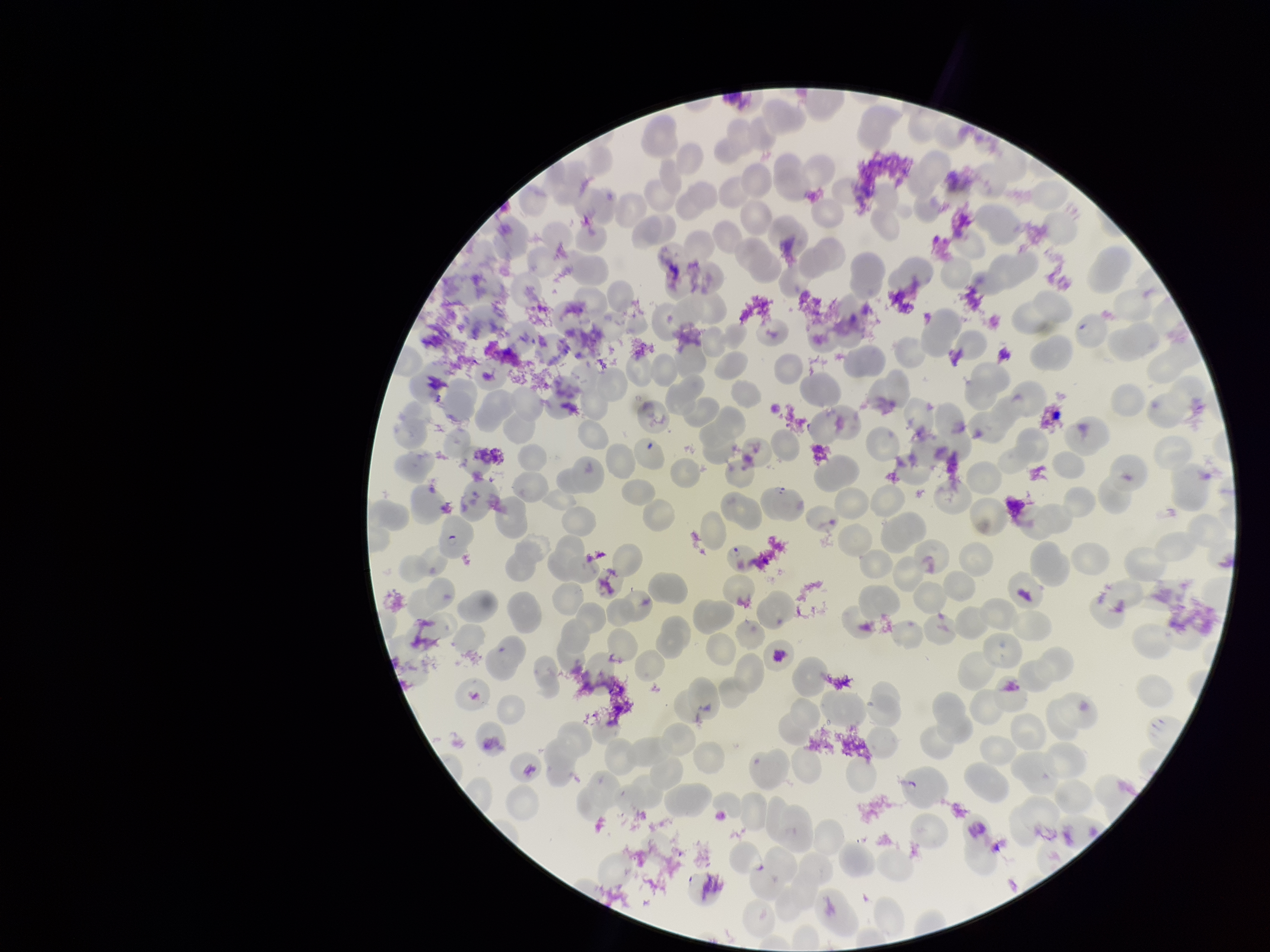
image_size: 1270×952 pixels
red_blood_cell_count: 269
parasitized_red_blood_cell_count: 2
species_reported_for_this_patient: Plasmodium falciparum
parasitized_red_blood_cells: detected
preparation: thin blood smear
patient_malaria_status: infected
stain: Giemsa
field_of_view: single
capture: smartphone photograph through the microscope eyepiece